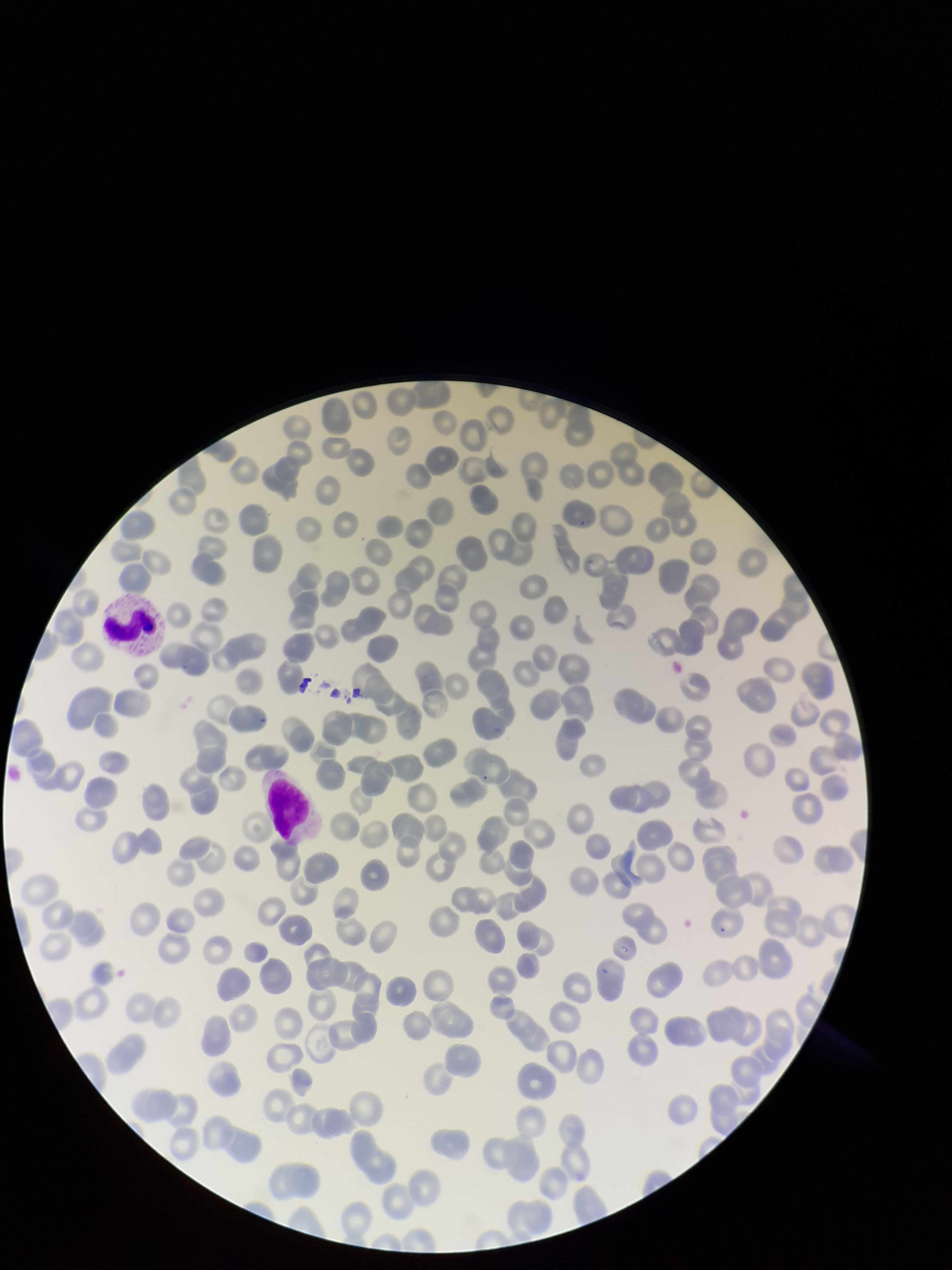
Red blood cell count: 211. Parasitized red blood cells: none identified. Species reported for this patient: Plasmodium falciparum. Photographed through the microscope eyepiece with a smartphone camera. Image is 952×1270 pixels. Patient malaria status: infected. Single field of view. Preparation: thin smear. Parasitized red blood cell count: 0. Stained with Giemsa.